Identify the preparation type.
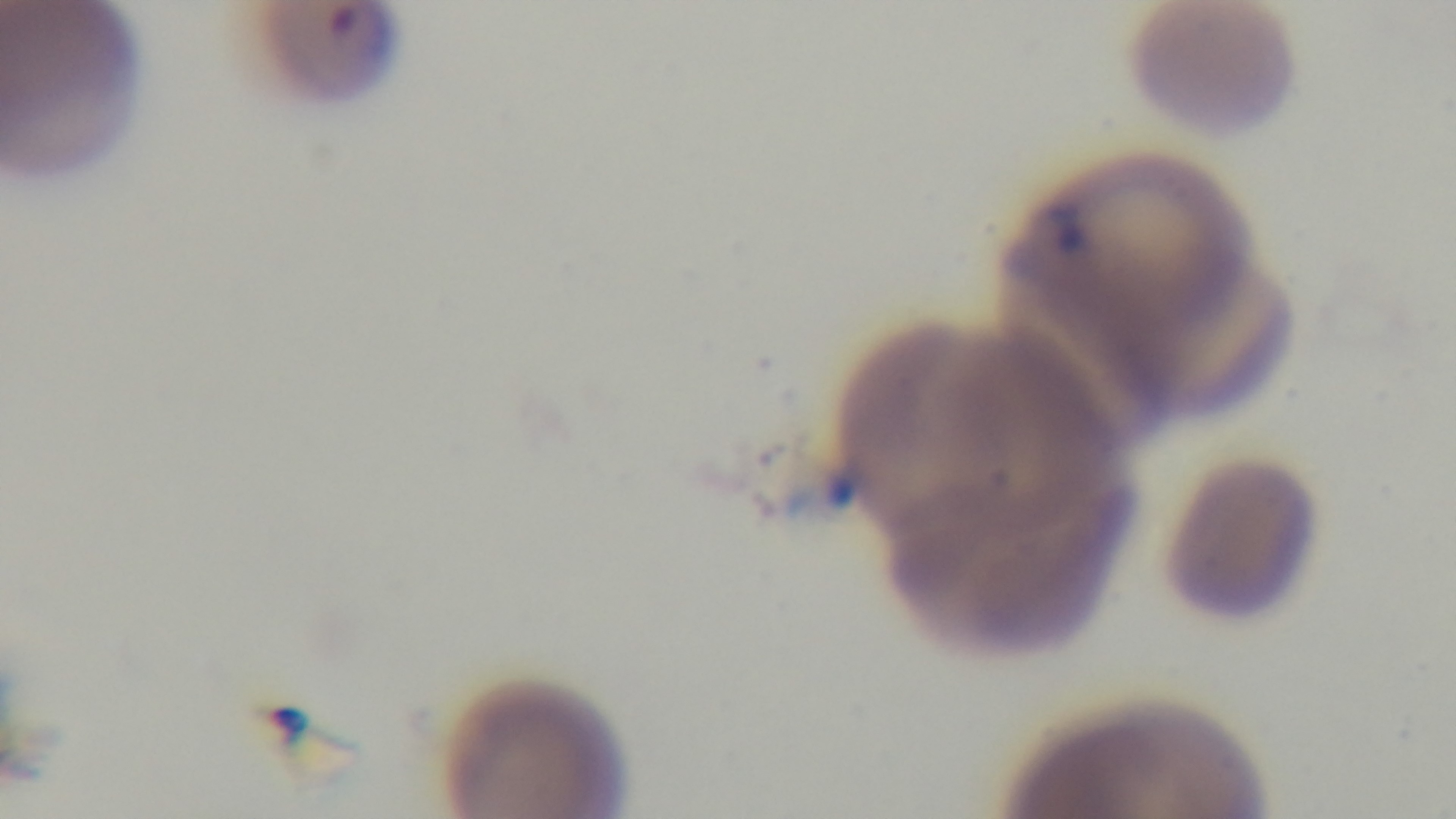
Thin.

100x oil-immersion objective. Giemsa stain. Captured with a mounted 4K digital camera. Single field of view. Malaria status: positive. Light microscopy.